Identify the cell.
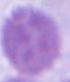

This is an erythrocyte.

{
  "modality": "photomicrograph",
  "magnification": "1000x"
}